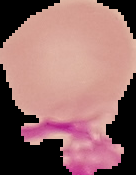

From a thin blood film. Cell region segmented out of the field of view; the surrounding area is masked to black. Malaria status: uninfected. Image is 136×175 pixels.